Identify the malaria species.
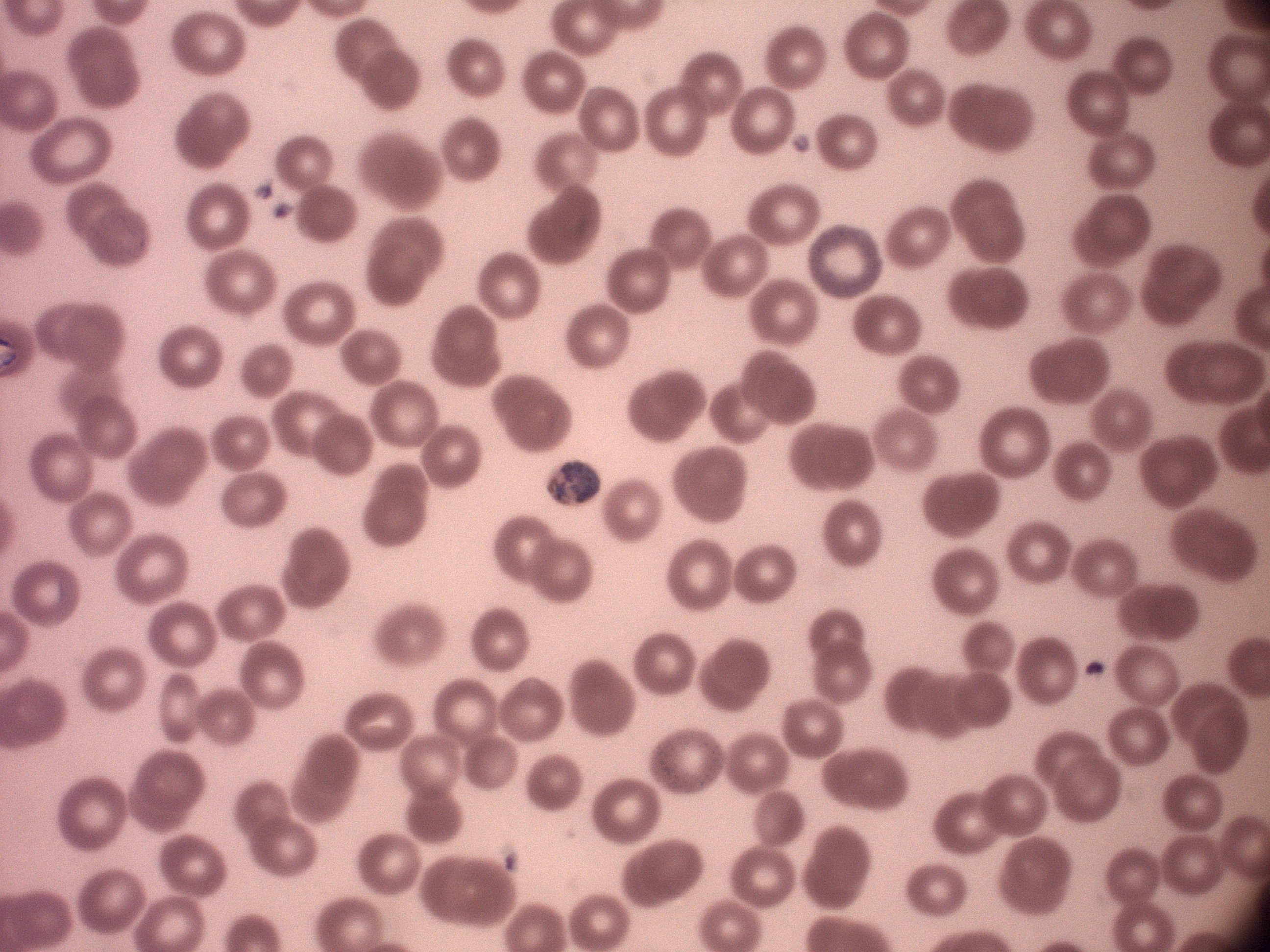
Plasmodium malariae.

Approximate bounding boxes as [x1, y1, x2, y2] in pixels, from the source annotation, which is not necessarily exhaustive.
Summary:
  - Trophozoite locations: [547, 462, 602, 504]
  - Field of view: one from this slide
  - Image size: 1270×952 pixels
  - Magnification: 100x
  - Stain: Giemsa
  - Preparation: thin blood smear
  - Microscope: Leica DM2000 with built-in camera